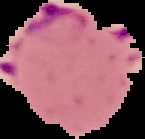
image type = segmented cell region on a black background
image size = 145×139 pixels
result = Plasmodium parasites identified
preparation = thin blood film